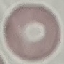

Malaria status: uninfected. Acquired by smartphone through the microscope eyepiece. Giemsa-stained preparation. Automatically extracted cell patch, resized to 64 × 64 pixels. Thin smear of blood.